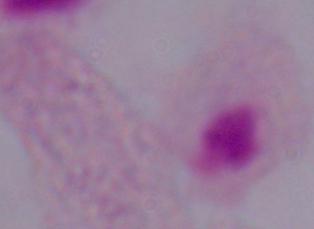

Summary:
  - Identification: trichomonad
  - Modality: micrograph
  - Magnification: 1000x